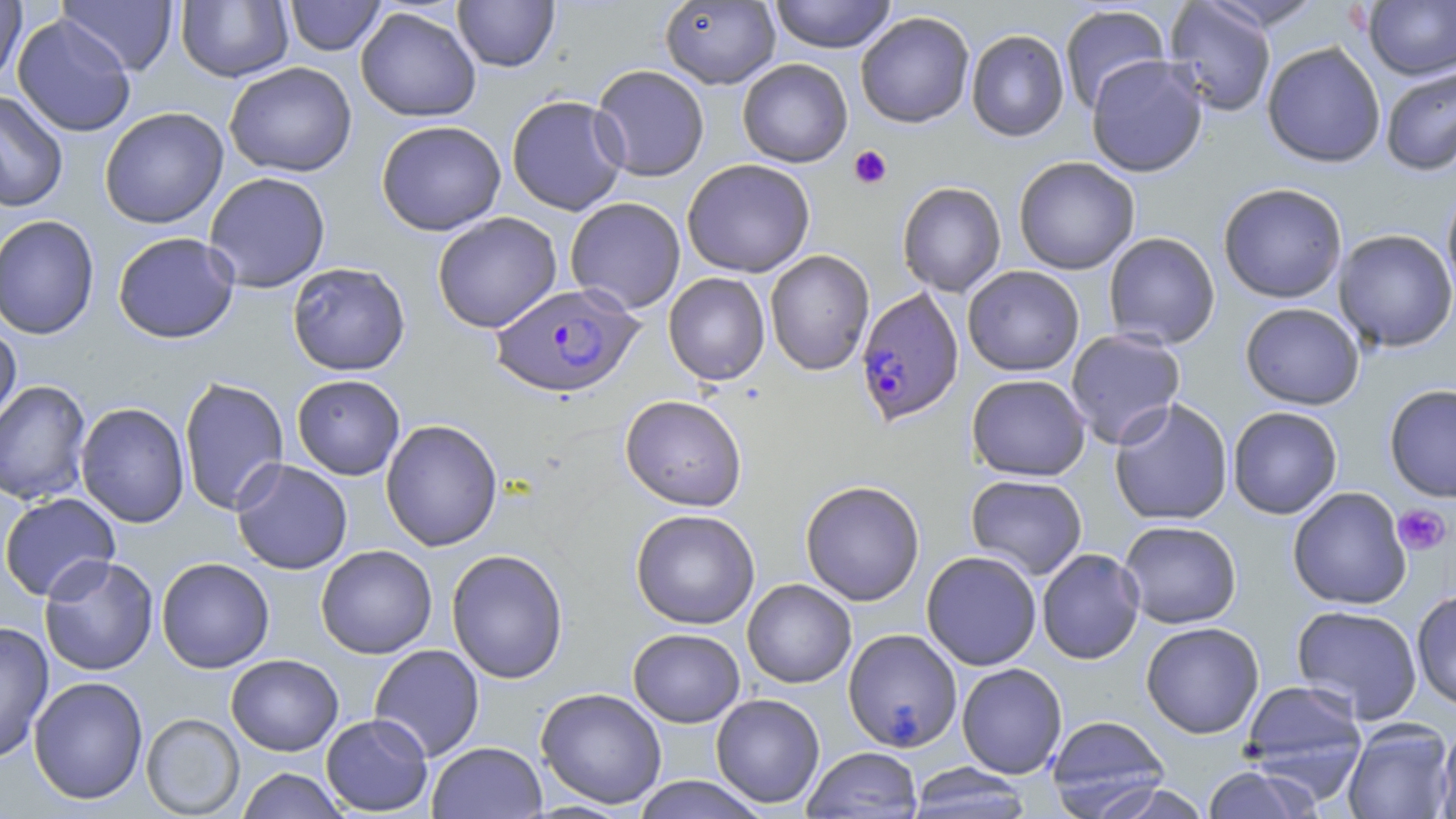
slide-level diagnosis = Plasmodium falciparum
image size = 1456×819 pixels
platelet locations = approximate bounding boxes as (x1,y1)-(x2,y2) corner pairs in pixels: (848,145)-(892,189), (1393,503)-(1450,556)
magnification = 1000x
Plasmodium falciparum-infected red blood cell locations = approximate bounding boxes as (x1,y1)-(x2,y2) corner pairs in pixels: (491,283)-(642,398), (855,288)-(964,425)
stain = May-Grünwald-Giemsa
field of view = one of a larger specimen
uninfected red blood cell locations = approximate bounding boxes as (x1,y1)-(x2,y2) corner pairs in pixels: (0,0)-(28,87), (284,0)-(386,56), (452,0)-(560,72), (768,0)-(898,53), (57,1)-(178,75), (176,1)-(293,82), (660,1)-(781,89), (1164,1)-(1277,117), (1363,1)-(1456,80), (1059,4)-(1171,115), (355,7)-(481,122), (855,11)-(975,128), (12,15)-(136,137), (966,29)-(1070,142), (1262,41)-(1386,168), (1086,56)-(1208,177), (737,58)-(853,168), (224,62)-(357,177), (590,64)-(710,181), (1380,66)-(1456,176), (0,91)-(69,211), (506,94)-(629,215), (99,107)-(229,229), (376,120)-(506,235), (1013,156)-(1140,275), (682,159)-(816,278), (204,172)-(331,292), (896,181)-(1006,297), (1441,182)-(1456,308), (1218,183)-(1347,303), (564,197)-(686,314), (432,212)-(562,333), (0,214)-(100,339), (1333,229)-(1456,353), (112,232)-(239,343), (1103,232)-(1220,349), (764,249)-(875,376), (287,262)-(411,376), (962,266)-(1085,376), (663,272)-(770,386), (1240,302)-(1364,410), (0,320)-(22,433), (1064,329)-(1186,449), (966,373)-(1091,481), (292,374)-(405,480), (178,376)-(290,516), (0,380)-(92,505), (1384,384)-(1456,502), (620,394)-(747,511), (1108,398)-(1233,526), (75,402)-(190,528), (1227,406)-(1343,519), (380,419)-(503,551), (230,458)-(353,575), (965,474)-(1088,579), (800,480)-(925,606), (1287,487)-(1412,610), (1,492)-(121,602), (630,508)-(760,630), (1118,520)-(1242,629), (315,544)-(437,659), (446,548)-(568,684), (1037,548)-(1145,664), (921,550)-(1042,670), (39,554)-(159,676), (156,557)-(274,673), (742,578)-(856,688), (1411,589)-(1456,711), (1291,604)-(1423,724), (0,622)-(54,763), (1140,622)-(1264,739), (628,628)-(745,727), (843,628)-(962,752), (369,644)-(485,761), (226,653)-(343,755), (956,662)-(1067,779), (28,676)-(148,804), (1241,679)-(1368,794), (535,687)-(667,809), (710,693)-(825,808), (141,713)-(245,818), (321,714)-(433,816), (1046,715)-(1171,817), (1342,720)-(1454,819), (1437,722)-(1456,819), (427,742)-(546,819), (802,746)-(923,818), (904,763)-(1036,819), (1201,765)-(1321,819), (236,768)-(348,818), (630,776)-(769,818), (1089,782)-(1214,819)
modality = light microscopy
preparation = thin blood smear